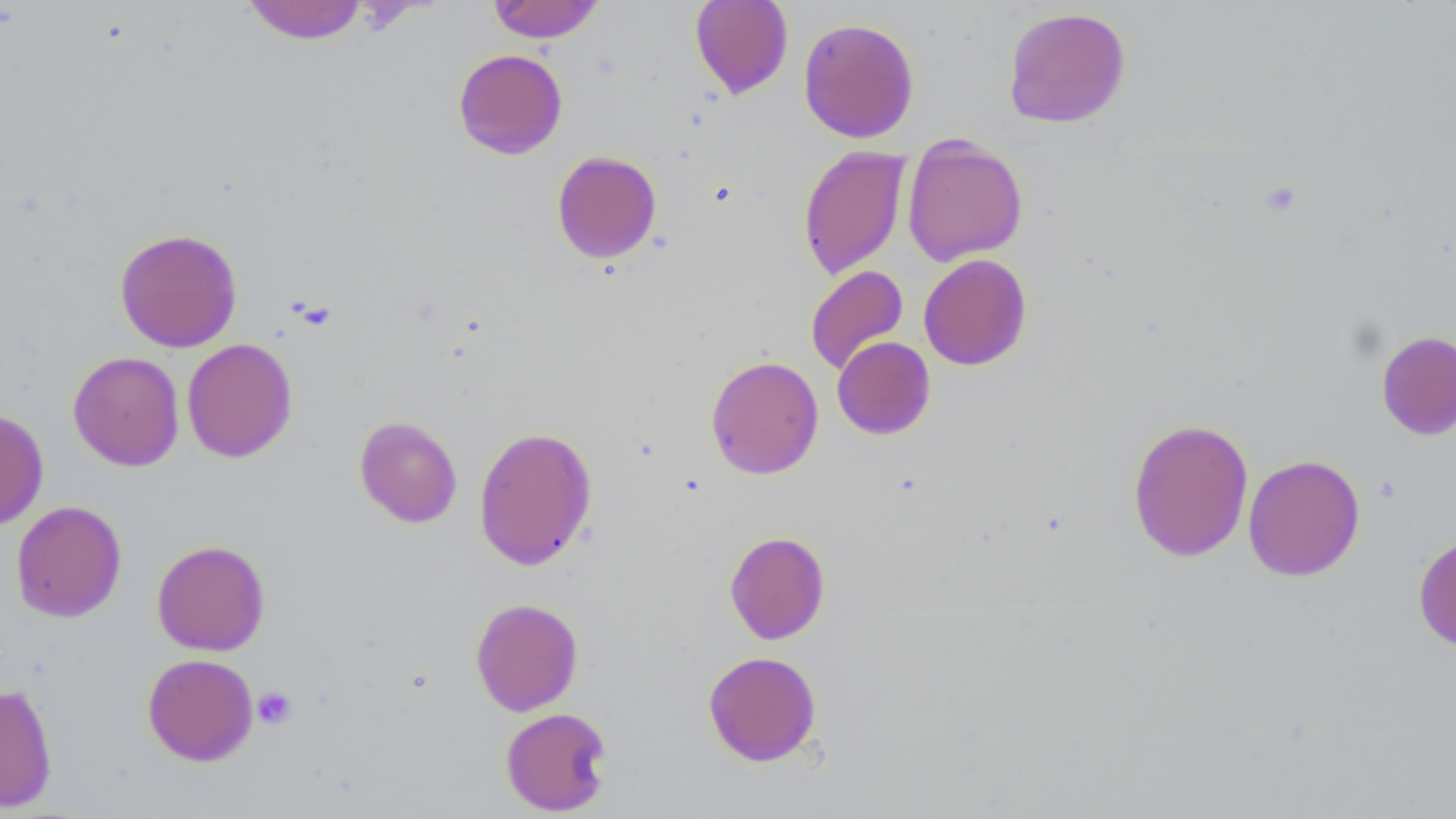
Summary:
  - Coordinate format: approximate bounding boxes as named x1/y1/x2/y2 corners in pixels
  - Uninfected red blood cell locations: (x1=690, y1=0, x2=793, y2=99), (x1=242, y1=1, x2=369, y2=44), (x1=488, y1=1, x2=605, y2=43), (x1=1003, y1=6, x2=1131, y2=129), (x1=798, y1=17, x2=920, y2=143), (x1=453, y1=49, x2=568, y2=160), (x1=902, y1=134, x2=1028, y2=266), (x1=797, y1=145, x2=910, y2=281), (x1=551, y1=150, x2=662, y2=264), (x1=114, y1=228, x2=243, y2=352), (x1=918, y1=253, x2=1032, y2=370), (x1=805, y1=265, x2=909, y2=376), (x1=1376, y1=330, x2=1456, y2=441), (x1=832, y1=336, x2=936, y2=439), (x1=182, y1=338, x2=297, y2=463), (x1=67, y1=351, x2=184, y2=471), (x1=706, y1=355, x2=824, y2=479), (x1=0, y1=407, x2=49, y2=530), (x1=354, y1=416, x2=463, y2=528), (x1=1127, y1=417, x2=1254, y2=562), (x1=473, y1=425, x2=597, y2=571), (x1=1242, y1=453, x2=1365, y2=582), (x1=10, y1=500, x2=127, y2=623), (x1=724, y1=531, x2=830, y2=644), (x1=1412, y1=533, x2=1456, y2=655), (x1=151, y1=539, x2=271, y2=656), (x1=470, y1=597, x2=584, y2=716), (x1=703, y1=650, x2=821, y2=766), (x1=142, y1=653, x2=258, y2=766), (x1=0, y1=683, x2=58, y2=812), (x1=500, y1=707, x2=613, y2=816)
  - Platelet locations: (x1=252, y1=686, x2=297, y2=730)
  - Slide-level diagnosis: no evidence of blood parasites
  - Field of view: single
  - Magnification: 1000x
  - Image size: 1456×819 pixels
  - Modality: light microscopy
  - Stain: May-Grünwald-Giemsa
  - Preparation: thin blood film